Locate every P. falciparum parasite and identify its life-cycle stage.
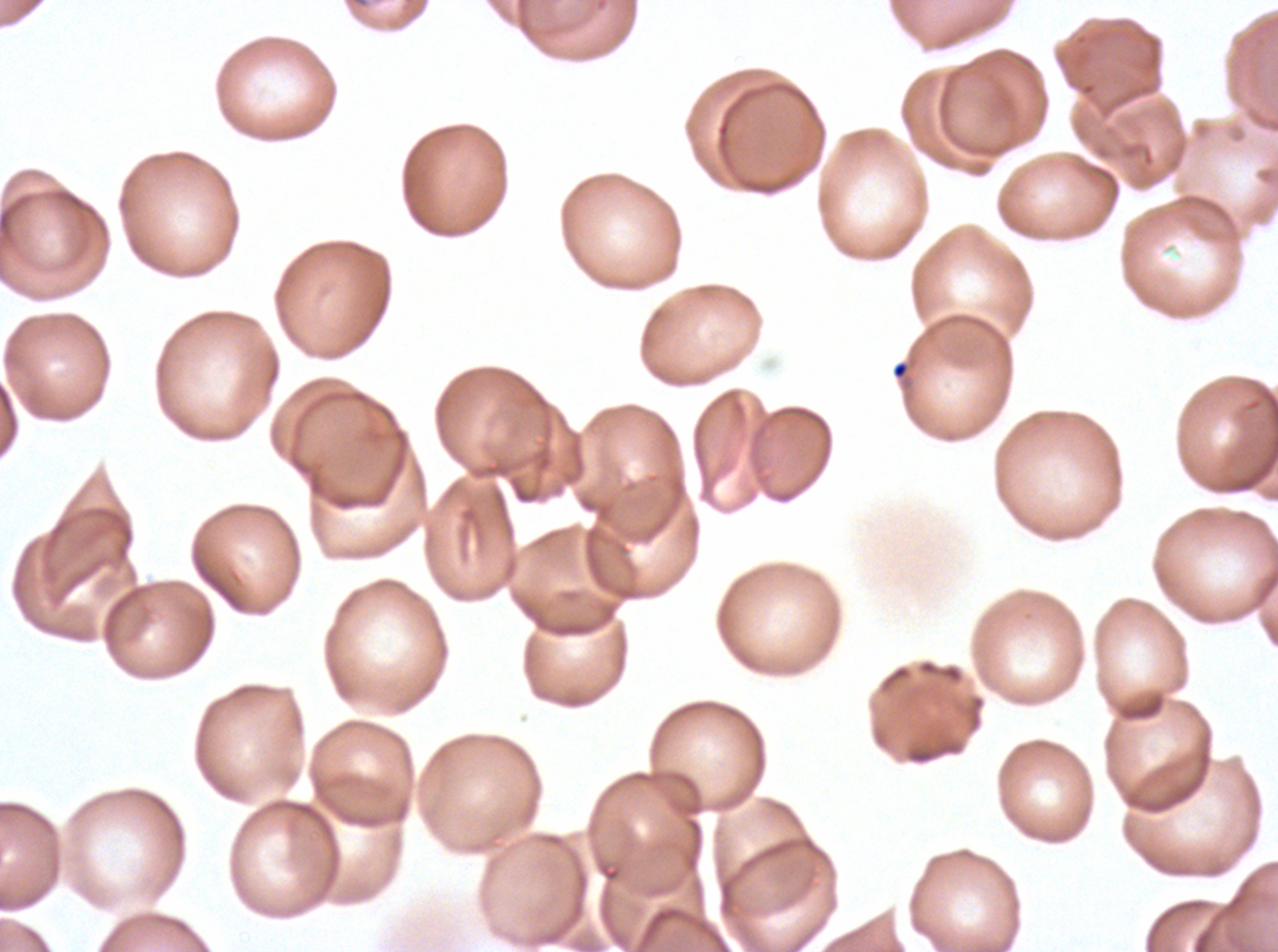
No rings, late-ring/early-trophozoite forms, mid trophozoites, late trophozoites, early schizonts, late schizonts, segmenters, or gametocytes observed.

Approximate bounding boxes as [x1, y1, x2, y2] in pixels. Debris locations: [891, 360, 911, 381]. One sub-image of a larger composite. Image is 1278×952 pixels. Giemsa-stained preparation. P. falciparum cultured ex vivo for 24 to 48 hours, from a patient in The Gambia. Thin blood film.